Assess this cell for malaria.
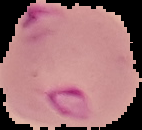
Parasitized.

Segmented cell region on a black background. Image is 142×130 pixels. From a thin blood film.